Assess this cell for malaria.
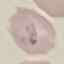
It is parasitized.

Summary:
  - Stain: Giemsa
  - Capture: smartphone through the microscope eyepiece
  - Preparation: thin blood film
  - Image type: cell patch, automatically extracted from a larger field of view and resized to 64 × 64 pixels